Locate every uninfected red blood cell.
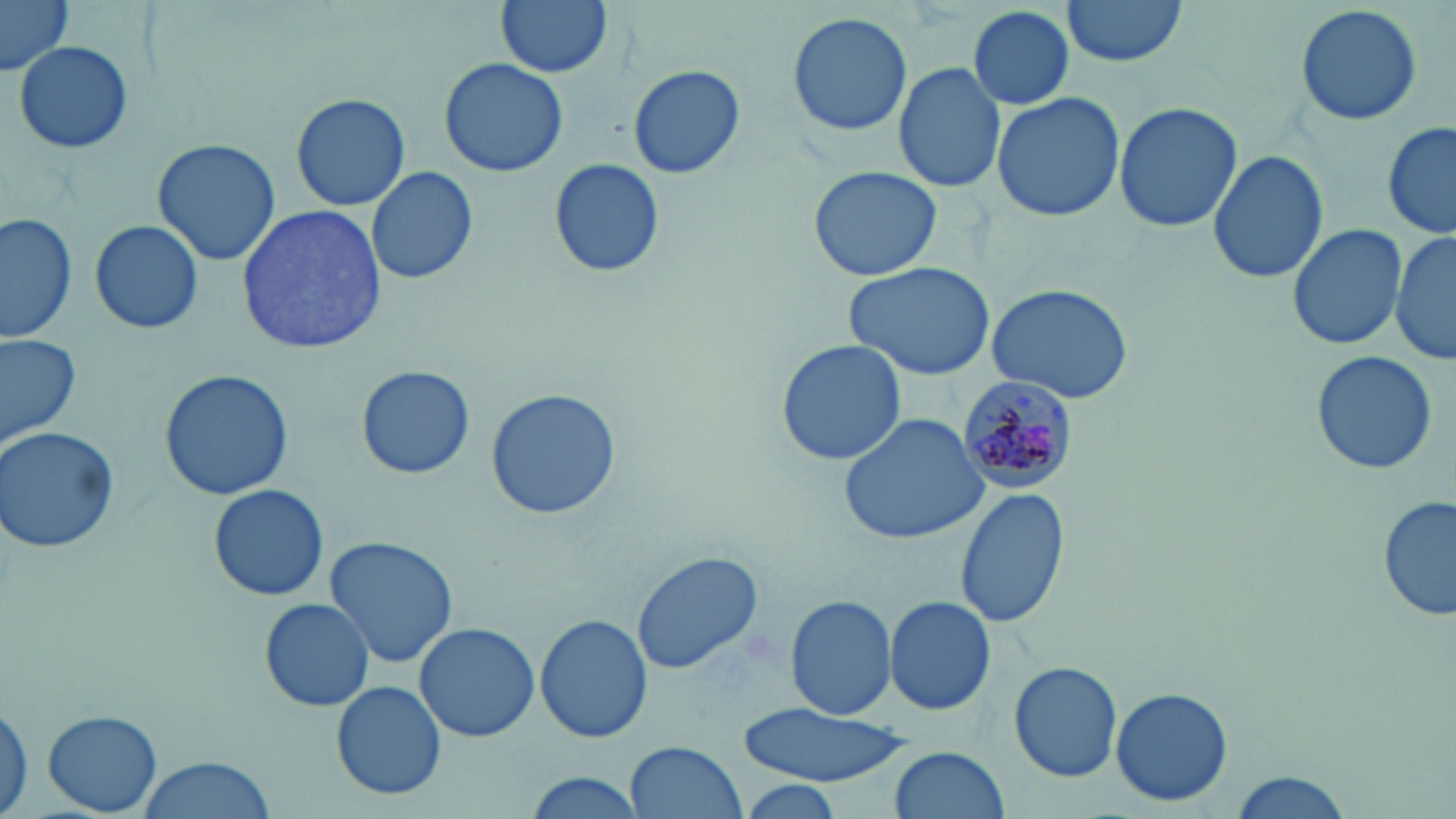

Approximate bounding boxes as (x1,y1)-(x2,y2) corner pairs in pixels.
Uninfected red blood cells: (495,0)-(613,78), (1062,0)-(1185,65), (0,1)-(72,75), (1295,2)-(1425,128), (967,5)-(1076,111), (786,12)-(913,137), (12,38)-(134,156), (438,58)-(568,177), (892,61)-(1008,194), (628,64)-(746,179), (991,90)-(1127,224), (290,94)-(409,211), (1113,99)-(1243,234), (1382,122)-(1455,242), (152,138)-(279,266), (1208,149)-(1328,284), (549,158)-(666,278), (367,165)-(478,285), (807,167)-(943,282), (237,204)-(386,354), (0,211)-(78,341), (89,217)-(204,336), (1288,221)-(1409,353), (1391,230)-(1455,365), (847,262)-(999,381), (987,280)-(1136,406), (0,331)-(81,446), (774,340)-(908,467), (1311,349)-(1438,476), (356,365)-(474,479), (158,369)-(294,501), (485,387)-(620,521), (839,413)-(991,545), (1,424)-(123,555), (208,484)-(329,602), (954,488)-(1070,630), (1378,495)-(1456,626), (326,534)-(457,667), (631,550)-(764,676), (786,594)-(899,719), (883,596)-(995,716), (259,598)-(374,712), (534,613)-(653,743), (414,622)-(540,743), (1009,662)-(1122,784), (332,681)-(446,801), (1110,688)-(1233,806), (0,692)-(33,819), (735,704)-(918,785), (44,710)-(162,815), (626,740)-(748,819), (886,746)-(1009,819), (137,755)-(276,819), (1226,770)-(1356,819), (522,771)-(652,819).

slide-level diagnosis = Plasmodium malariae
modality = light microscopy
Plasmodium malariae-infected red blood cell locations = approximate bounding boxes as (x1,y1)-(x2,y2) corner pairs in pixels: (956,372)-(1080,492)
image size = 1456×819 pixels
stain = May-Grünwald-Giemsa
field of view = one of a larger specimen
preparation = thin blood smear
magnification = 1000x